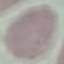
Malaria status: uninfected. Thin blood film. Cell patch, automatically extracted from a larger field of view and resized to 64 × 64 pixels. Giemsa stain. Acquired by smartphone through the microscope eyepiece.